Classify this cell by malaria status.
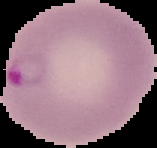
It is parasitized.

Summary:
  - Image type: segmented cell region with the area outside set to black
  - Preparation: thin blood film
  - Image size: 157×148 pixels